State which parasite is depicted.
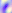
Toxoplasma gondii.

Summary:
  - Modality: micrograph
  - Magnification: 400x